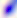

Summary:
  - Identification: Toxoplasma gondii
  - Modality: photomicrograph
  - Magnification: 400x